Name the blood parasite species.
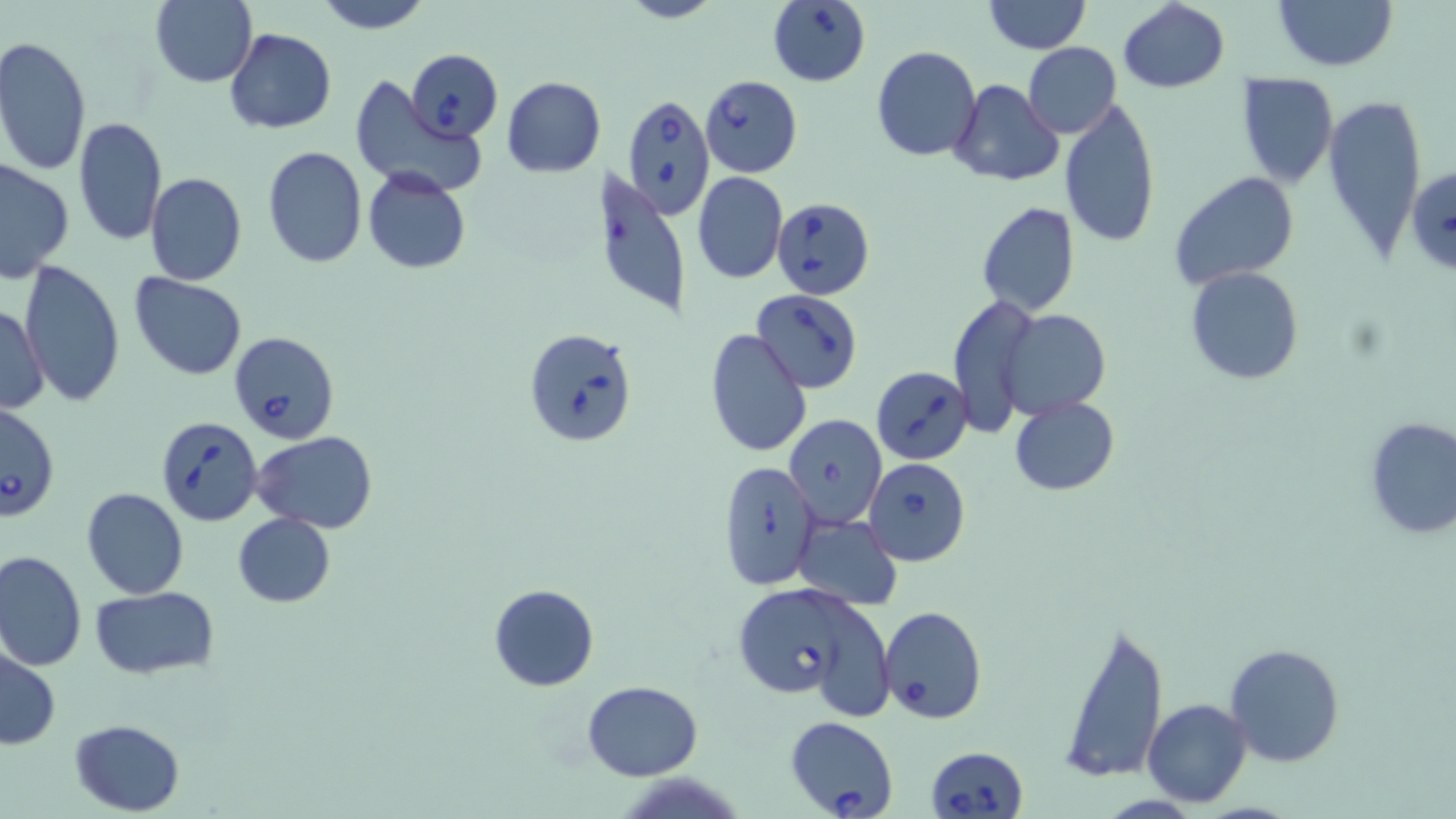

Babesia divergens.

Approximate bounding boxes as named x1/y1/x2/y2 corners in pixels. Uninfected red blood cell locations: (x1=150, y1=0, x2=257, y2=88), (x1=311, y1=0, x2=434, y2=34), (x1=614, y1=0, x2=722, y2=24), (x1=981, y1=0, x2=1092, y2=53), (x1=1117, y1=0, x2=1230, y2=92), (x1=1270, y1=0, x2=1398, y2=73), (x1=225, y1=27, x2=336, y2=134), (x1=1, y1=35, x2=94, y2=176), (x1=1023, y1=41, x2=1122, y2=138), (x1=871, y1=47, x2=981, y2=162), (x1=1234, y1=71, x2=1339, y2=188), (x1=501, y1=75, x2=605, y2=177), (x1=350, y1=76, x2=482, y2=197), (x1=950, y1=80, x2=1064, y2=186), (x1=1323, y1=94, x2=1424, y2=264), (x1=1059, y1=97, x2=1161, y2=249), (x1=73, y1=114, x2=169, y2=246), (x1=261, y1=146, x2=367, y2=269), (x1=0, y1=157, x2=77, y2=285), (x1=362, y1=167, x2=472, y2=274), (x1=692, y1=171, x2=787, y2=283), (x1=144, y1=172, x2=247, y2=287), (x1=1168, y1=172, x2=1298, y2=290), (x1=596, y1=173, x2=690, y2=320), (x1=975, y1=202, x2=1080, y2=317), (x1=19, y1=259, x2=127, y2=408), (x1=1185, y1=267, x2=1305, y2=384), (x1=130, y1=273, x2=247, y2=379), (x1=948, y1=294, x2=1036, y2=436), (x1=0, y1=304, x2=48, y2=413), (x1=993, y1=308, x2=1111, y2=420), (x1=704, y1=328, x2=812, y2=461), (x1=1009, y1=397, x2=1119, y2=495), (x1=1361, y1=418, x2=1456, y2=538), (x1=252, y1=432, x2=377, y2=533), (x1=719, y1=462, x2=819, y2=591), (x1=81, y1=487, x2=189, y2=600), (x1=232, y1=512, x2=336, y2=606), (x1=793, y1=514, x2=903, y2=608), (x1=0, y1=550, x2=86, y2=672), (x1=488, y1=583, x2=598, y2=692), (x1=88, y1=587, x2=221, y2=678), (x1=1057, y1=615, x2=1168, y2=787), (x1=1225, y1=643, x2=1346, y2=767), (x1=1, y1=647, x2=60, y2=750), (x1=581, y1=680, x2=704, y2=781), (x1=1143, y1=697, x2=1252, y2=806), (x1=69, y1=719, x2=187, y2=815). Babesia divergens-infected red blood cell locations: (x1=767, y1=1, x2=871, y2=86), (x1=406, y1=49, x2=503, y2=143), (x1=700, y1=74, x2=802, y2=177), (x1=621, y1=93, x2=714, y2=221), (x1=1408, y1=167, x2=1455, y2=276), (x1=771, y1=197, x2=874, y2=299), (x1=753, y1=290, x2=862, y2=392), (x1=522, y1=327, x2=637, y2=448), (x1=226, y1=329, x2=340, y2=445), (x1=871, y1=366, x2=974, y2=464), (x1=1, y1=404, x2=61, y2=523), (x1=783, y1=413, x2=887, y2=528), (x1=156, y1=414, x2=264, y2=525), (x1=864, y1=458, x2=970, y2=567), (x1=729, y1=582, x2=885, y2=706), (x1=880, y1=606, x2=986, y2=724), (x1=785, y1=715, x2=900, y2=819), (x1=924, y1=746, x2=1028, y2=819). May-Grünwald-Giemsa stain. Optical microscopy. Single field of view. Thin blood smear. Image is 1456×819 pixels. Captured at 1000x magnification.